Outline each Babesia divergens-infected red blood cell.
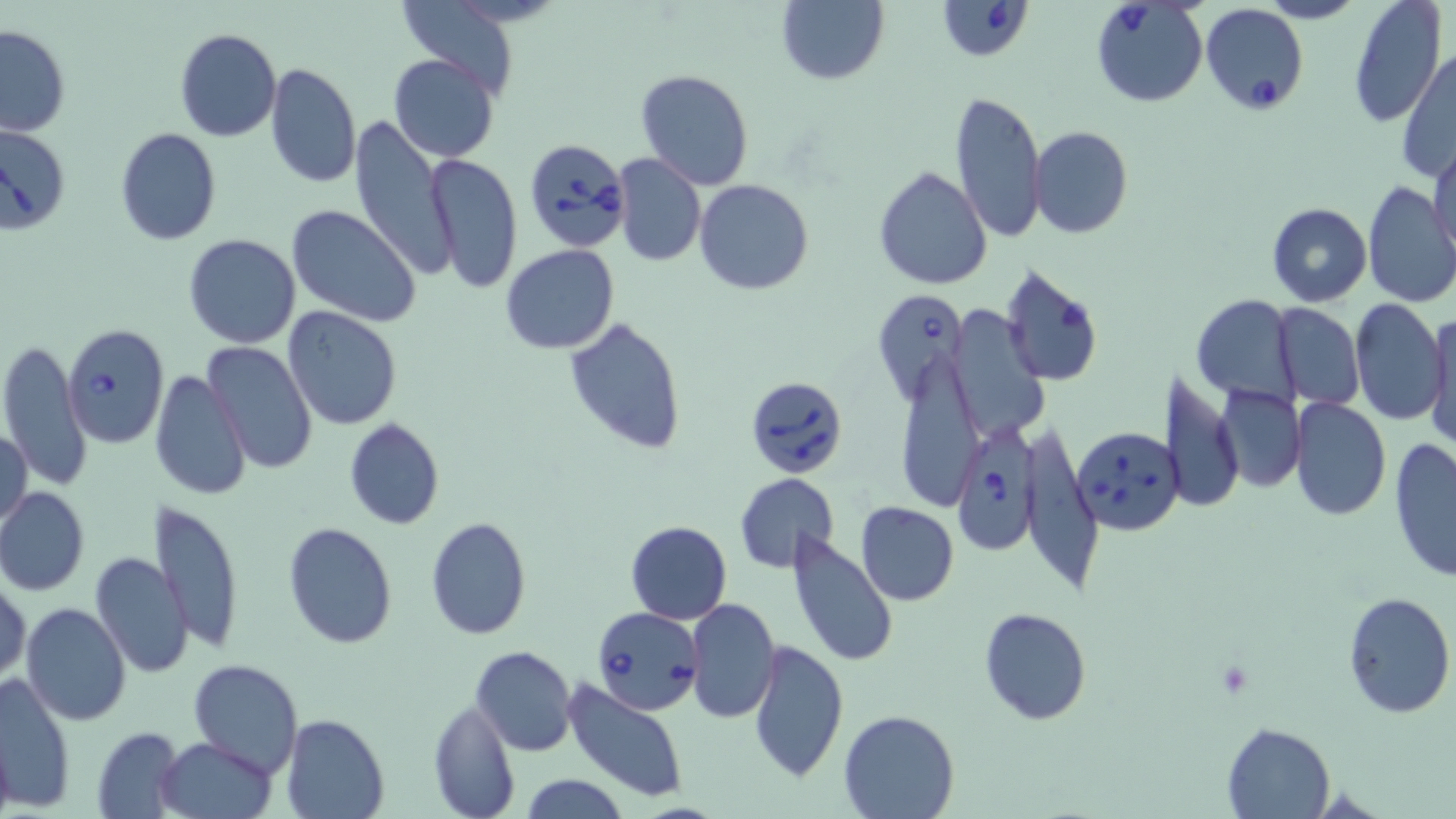
Approximate bounding boxes as named x1/y1/x2/y2 corners in pixels.
Babesia divergens-infected red blood cells: (x1=937, y1=0, x2=1032, y2=61), (x1=1090, y1=2, x2=1209, y2=108), (x1=1200, y1=2, x2=1311, y2=117), (x1=0, y1=123, x2=71, y2=235), (x1=523, y1=138, x2=630, y2=252), (x1=869, y1=289, x2=969, y2=403), (x1=63, y1=325, x2=172, y2=450), (x1=751, y1=378, x2=843, y2=476), (x1=954, y1=414, x2=1039, y2=552), (x1=1071, y1=425, x2=1184, y2=535), (x1=594, y1=606, x2=703, y2=715).

Uninfected red blood cell locations: (x1=776, y1=0, x2=889, y2=87), (x1=1346, y1=0, x2=1445, y2=129), (x1=395, y1=2, x2=525, y2=99), (x1=0, y1=24, x2=72, y2=137), (x1=174, y1=29, x2=282, y2=143), (x1=201, y1=37, x2=331, y2=157), (x1=1397, y1=48, x2=1456, y2=185), (x1=389, y1=53, x2=499, y2=161), (x1=265, y1=63, x2=361, y2=188), (x1=635, y1=68, x2=755, y2=191), (x1=948, y1=88, x2=1045, y2=242), (x1=348, y1=118, x2=455, y2=280), (x1=1029, y1=125, x2=1133, y2=239), (x1=114, y1=128, x2=222, y2=245), (x1=1428, y1=137, x2=1455, y2=260), (x1=425, y1=152, x2=523, y2=294), (x1=612, y1=153, x2=705, y2=268), (x1=874, y1=165, x2=993, y2=290), (x1=695, y1=178, x2=813, y2=295), (x1=1361, y1=182, x2=1455, y2=311), (x1=1267, y1=202, x2=1372, y2=307), (x1=286, y1=204, x2=422, y2=327), (x1=182, y1=233, x2=302, y2=349), (x1=500, y1=245, x2=620, y2=354), (x1=1001, y1=264, x2=1105, y2=386), (x1=1191, y1=294, x2=1300, y2=409), (x1=1350, y1=298, x2=1449, y2=426), (x1=1272, y1=304, x2=1363, y2=409), (x1=284, y1=307, x2=401, y2=429), (x1=1425, y1=307, x2=1456, y2=453), (x1=954, y1=308, x2=1042, y2=439), (x1=564, y1=316, x2=688, y2=454), (x1=0, y1=337, x2=92, y2=492), (x1=204, y1=341, x2=317, y2=476), (x1=895, y1=353, x2=986, y2=512), (x1=150, y1=368, x2=254, y2=502), (x1=1160, y1=373, x2=1243, y2=512), (x1=1215, y1=383, x2=1306, y2=491), (x1=1289, y1=396, x2=1390, y2=521), (x1=343, y1=419, x2=445, y2=530), (x1=1, y1=424, x2=33, y2=532), (x1=1017, y1=427, x2=1107, y2=587), (x1=1388, y1=437, x2=1456, y2=583), (x1=734, y1=473, x2=839, y2=573), (x1=0, y1=487, x2=90, y2=595), (x1=150, y1=499, x2=246, y2=654), (x1=855, y1=501, x2=959, y2=604), (x1=425, y1=518, x2=531, y2=639), (x1=625, y1=520, x2=731, y2=625), (x1=283, y1=522, x2=397, y2=648), (x1=787, y1=531, x2=898, y2=670), (x1=90, y1=552, x2=194, y2=677), (x1=1, y1=573, x2=28, y2=687), (x1=1341, y1=592, x2=1455, y2=719), (x1=686, y1=598, x2=781, y2=722), (x1=22, y1=602, x2=131, y2=727), (x1=978, y1=607, x2=1091, y2=724), (x1=747, y1=638, x2=849, y2=783), (x1=470, y1=645, x2=578, y2=756), (x1=187, y1=659, x2=304, y2=774), (x1=0, y1=672, x2=75, y2=812), (x1=565, y1=678, x2=691, y2=803), (x1=428, y1=699, x2=520, y2=819), (x1=838, y1=708, x2=959, y2=819), (x1=280, y1=713, x2=389, y2=818), (x1=1222, y1=722, x2=1334, y2=818), (x1=91, y1=727, x2=184, y2=816), (x1=155, y1=736, x2=277, y2=819), (x1=518, y1=773, x2=629, y2=819). Slide-level diagnosis: Babesia divergens. Single field of view. Image is 1456×819 pixels. Thin blood smear. Optical microscopy. May-Grünwald-Giemsa-stained preparation. 1000x magnification.